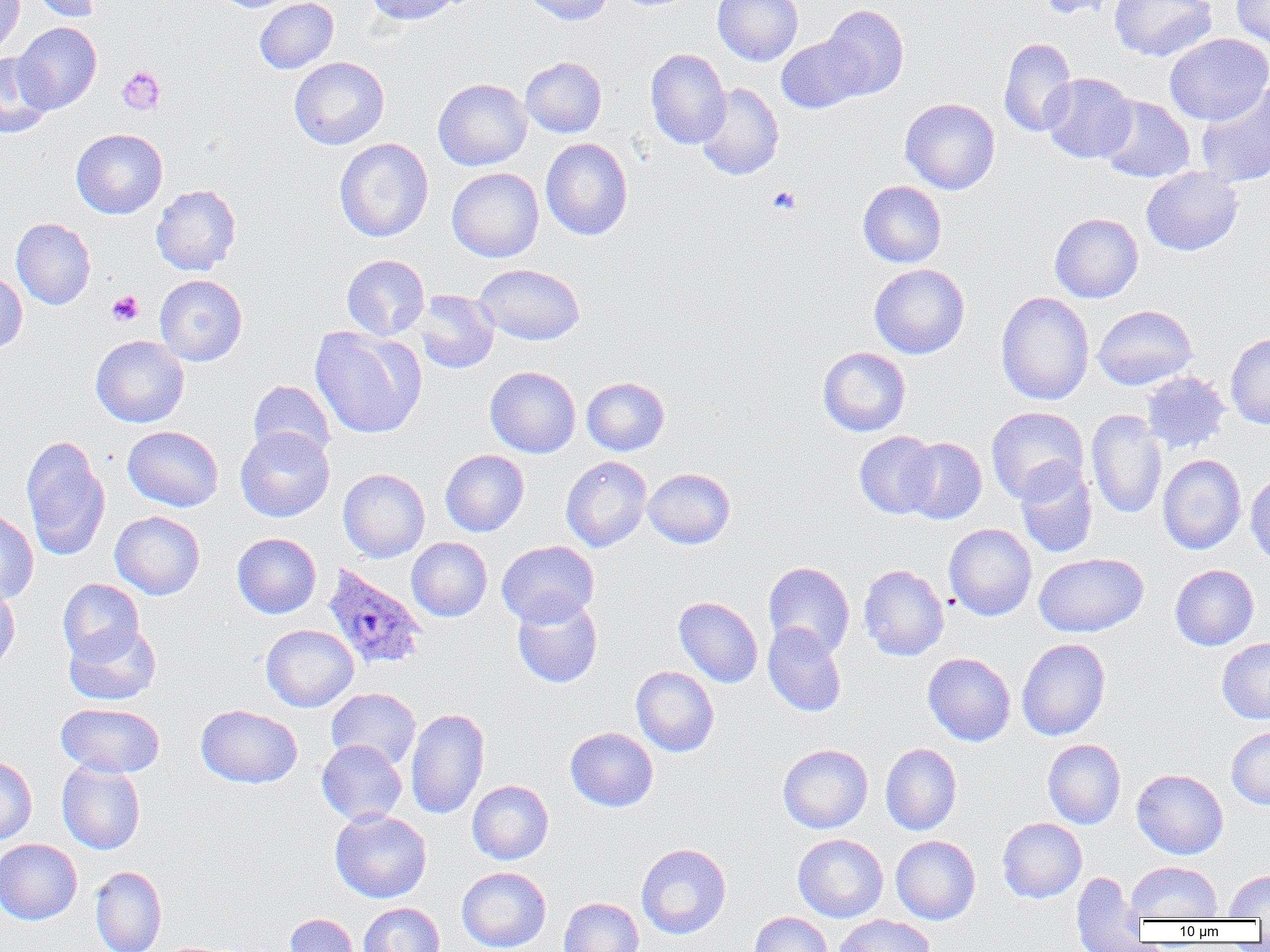
{
  "slide_level_diagnosis": "Plasmodium ovale",
  "field_of_view": "one of a larger specimen",
  "uninfected_red_blood_cell_locations": "approximate bounding boxes as (x1,y1)-(x2,y2) corner pairs in pixels: (0,0)-(24,59), (27,0)-(103,22), (215,0)-(299,12), (254,0)-(339,74), (365,0)-(463,25), (522,0)-(612,26), (712,0)-(803,66), (1037,0)-(1126,20), (1109,0)-(1217,62), (1231,0)-(1270,51), (820,4)-(909,100), (12,21)-(102,113), (1164,33)-(1270,125), (776,36)-(868,113), (999,37)-(1078,137), (645,48)-(731,149), (0,53)-(52,138), (520,56)-(607,138), (289,57)-(390,150), (1041,73)-(1137,163), (433,78)-(532,171), (694,82)-(784,180), (1194,83)-(1270,187), (1097,95)-(1194,183), (900,97)-(1000,195), (71,129)-(167,218), (334,138)-(433,243), (540,138)-(633,241), (1141,167)-(1243,256), (447,168)-(544,262), (858,181)-(947,268), (151,184)-(241,275), (1049,213)-(1143,303), (11,217)-(96,310), (341,254)-(430,340), (869,263)-(969,359), (473,264)-(585,345), (0,270)-(27,354), (155,274)-(247,366), (412,290)-(499,374), (995,291)-(1095,405), (1093,304)-(1197,390), (310,326)-(426,439), (1226,332)-(1270,429), (90,335)-(189,427), (817,347)-(911,436), (484,366)-(580,458), (1141,371)-(1230,453), (582,376)-(669,455), (248,380)-(335,463), (986,406)-(1088,503), (1086,409)-(1167,519), (122,426)-(223,511), (235,427)-(334,522), (854,431)-(940,518), (20,435)-(111,560), (900,437)-(987,524), (440,450)-(529,536), (1157,454)-(1246,555), (560,456)-(651,552), (1015,460)-(1098,558), (338,468)-(430,562), (643,468)-(735,549), (1245,473)-(1270,566), (0,508)-(39,605), (110,511)-(205,599), (944,523)-(1037,621), (232,533)-(321,618), (406,537)-(492,622), (497,541)-(598,628), (1034,553)-(1149,637), (763,561)-(855,659), (858,564)-(949,661), (1169,564)-(1259,650), (58,578)-(144,662), (0,580)-(20,676), (512,593)-(603,688), (673,596)-(763,688), (64,623)-(161,706), (763,623)-(847,717), (261,624)-(359,712), (1016,638)-(1111,741), (1217,638)-(1270,724), (923,652)-(1015,746), (631,666)-(719,756), (326,688)-(421,770), (55,703)-(165,778), (196,704)-(302,788), (405,707)-(490,819), (565,727)-(659,812), (1226,727)-(1270,809), (1042,739)-(1126,829), (316,740)-(407,825), (777,743)-(873,834), (880,743)-(962,835), (0,756)-(37,844), (56,760)-(146,854), (1131,769)-(1229,859), (467,780)-(554,865), (329,809)-(431,903), (997,817)-(1087,903), (793,834)-(888,923), (891,835)-(980,925), (0,839)-(82,925), (636,843)-(731,939), (1126,861)-(1223,922), (90,865)-(167,952), (456,866)-(551,952), (1224,870)-(1270,919), (1071,871)-(1146,951), (559,897)-(644,952), (358,903)-(444,952), (749,912)-(833,952), (285,913)-(358,952), (833,914)-(934,952)",
  "platelet_locations": "approximate bounding boxes as (x1,y1)-(x2,y2) corner pairs in pixels: (117,66)-(165,115), (768,186)-(801,214), (107,290)-(143,326)",
  "image_size": "1270×952 pixels",
  "modality": "optical microscopy",
  "preparation": "thin blood smear",
  "plasmodium_ovale_infected_red_blood_cell_locations": "approximate bounding boxes as (x1,y1)-(x2,y2) corner pairs in pixels: (322,563)-(426,670)",
  "magnification": "1000x"
}